Report the malaria status of this cell.
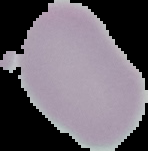
It is uninfected.

Summary:
  - Preparation: thin blood smear
  - Image size: 148×151 pixels
  - Image type: segmented cell region on a black background